Outline every malaria parasite.
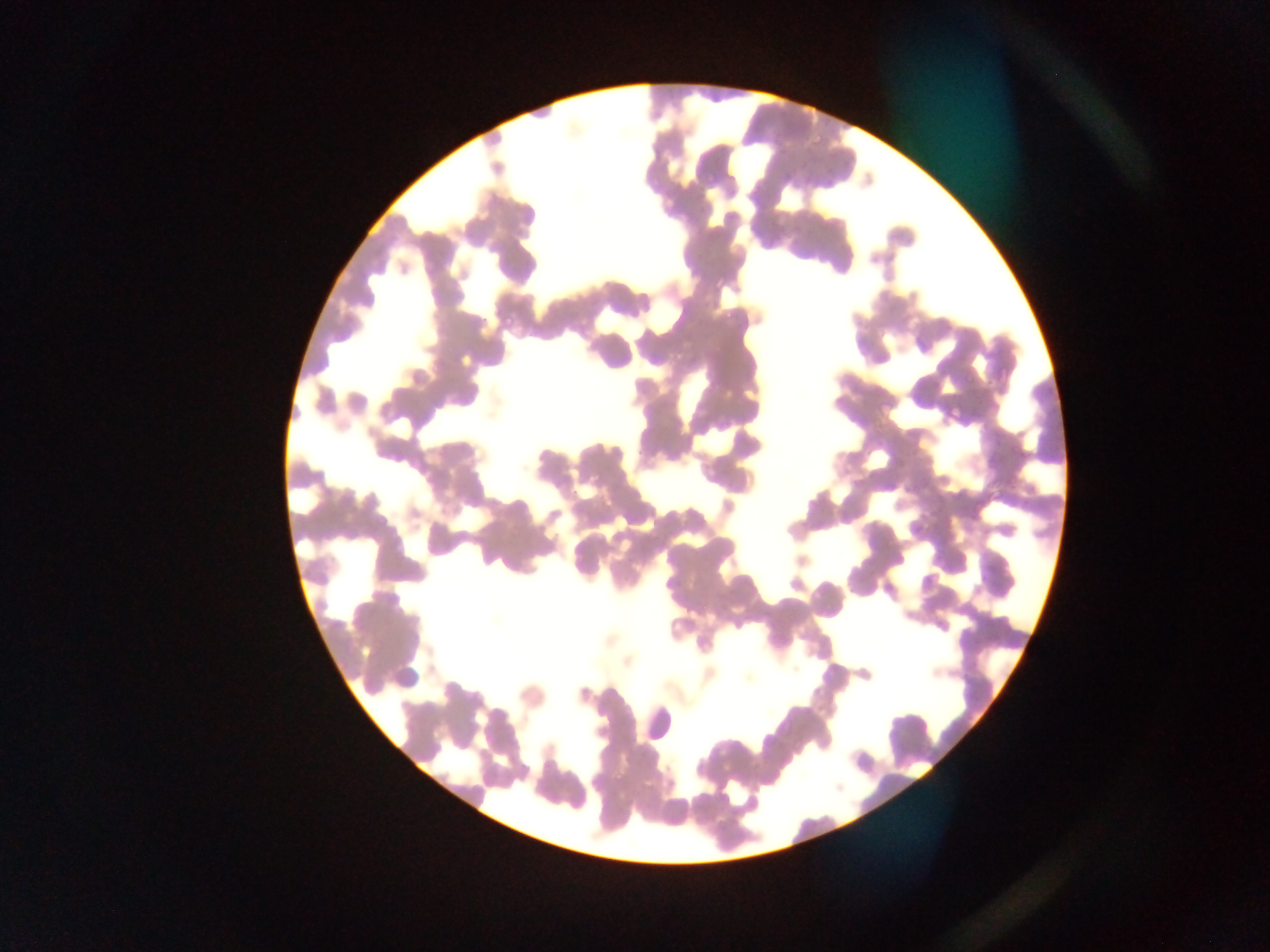

Approximate bounding boxes as [left, top, right, bottom] in pixels.
Malaria parasites: [811, 133, 824, 147], [779, 169, 793, 184], [703, 171, 717, 186], [646, 176, 657, 187], [723, 178, 738, 197], [823, 179, 834, 190], [712, 275, 726, 290], [720, 306, 737, 322], [500, 312, 516, 328], [946, 403, 964, 421], [508, 524, 523, 537], [612, 773, 626, 787].

Sample from Ghana. Thin blood smear. Mobile-phone photograph taken through the microscope. Image is 1270×952 pixels. One field of view.